Evaluate for malaria.
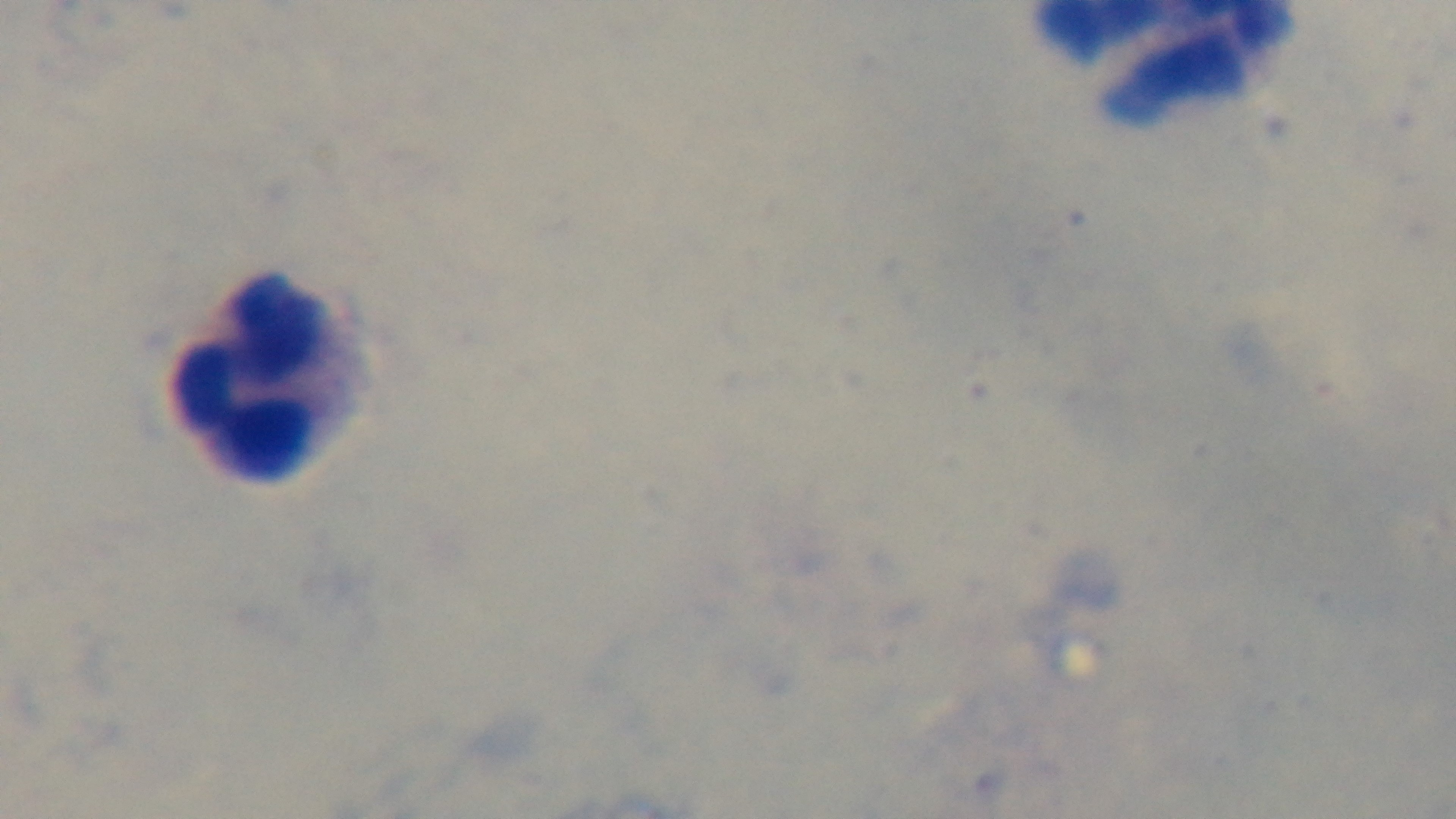

It is uninfected.

Preparation: thick smear. Light microscopy. Giemsa stain. Single field of view. Oil-immersion objective, 100x. Captured with a mounted 4K digital camera.